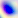
modality = micrograph
magnification = 400x
identification = Toxoplasma gondii